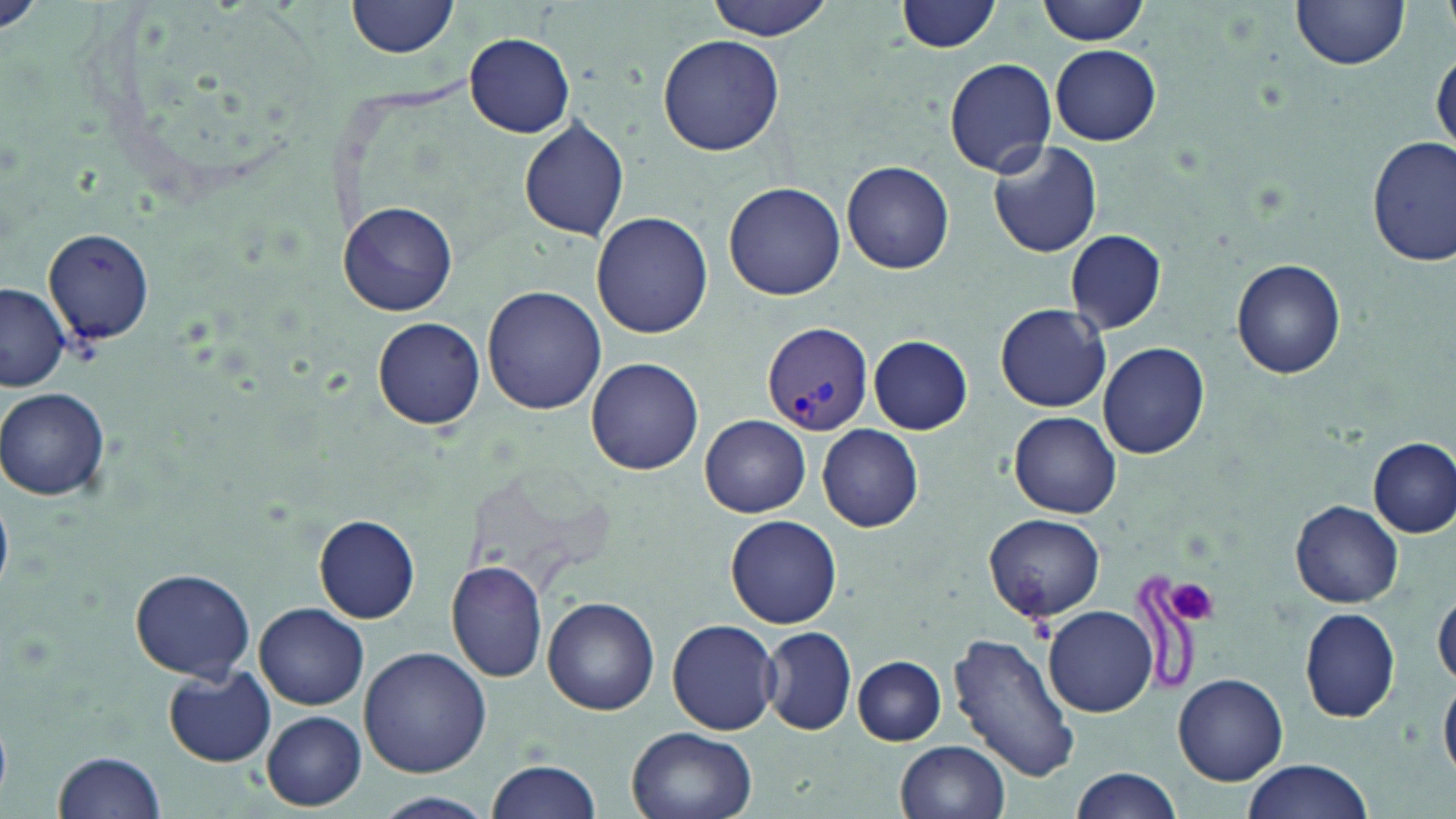

slide-level diagnosis = Plasmodium vivax
preparation = thin blood film
modality = optical microscopy
image size = 1456×819 pixels
Plasmodium vivax-infected red blood cell locations = approximate bounding boxes as (x1, y1, x2, y2) in pixels: (760, 322, 874, 437)
platelet locations = approximate bounding boxes as (x1, y1, x2, y2) in pixels: (1166, 577, 1218, 627)
uninfected red blood cell locations = approximate bounding boxes as (x1, y1, x2, y2) in pixels: (347, 0, 462, 60), (706, 0, 837, 41), (896, 0, 1004, 54), (1038, 0, 1152, 46), (1290, 1, 1410, 71), (464, 33, 575, 137), (658, 33, 785, 157), (1049, 44, 1162, 146), (1431, 52, 1455, 156), (944, 59, 1056, 175), (518, 116, 630, 242), (1368, 137, 1454, 265), (987, 140, 1103, 258), (843, 161, 954, 273), (723, 182, 846, 301), (340, 201, 456, 315), (592, 211, 712, 338), (38, 228, 156, 346), (1065, 229, 1166, 335), (1230, 259, 1347, 380), (482, 284, 607, 414), (0, 286, 71, 391), (997, 303, 1111, 414), (373, 317, 485, 429), (868, 334, 972, 434), (1098, 342, 1208, 459), (586, 358, 703, 473), (1, 388, 111, 501), (1010, 412, 1120, 518), (700, 415, 810, 517), (817, 424, 923, 533), (1369, 437, 1455, 538), (1291, 501, 1403, 607), (984, 513, 1106, 621), (315, 514, 422, 622), (726, 514, 842, 628), (448, 561, 549, 682), (128, 568, 256, 682), (1433, 588, 1456, 688), (543, 598, 660, 716), (256, 603, 370, 711), (1044, 604, 1158, 717), (1299, 608, 1402, 722), (667, 617, 780, 735), (759, 626, 857, 735), (951, 631, 1080, 782), (359, 647, 491, 777), (852, 657, 946, 745), (165, 666, 276, 767), (1440, 670, 1456, 782), (1173, 673, 1288, 785), (262, 711, 367, 810), (627, 729, 756, 819), (896, 739, 1009, 819), (53, 750, 166, 819), (1237, 758, 1376, 819), (487, 759, 603, 819), (1067, 765, 1184, 819), (373, 792, 497, 819)
magnification = 1000x
stain = May-Grünwald-Giemsa
field of view = single